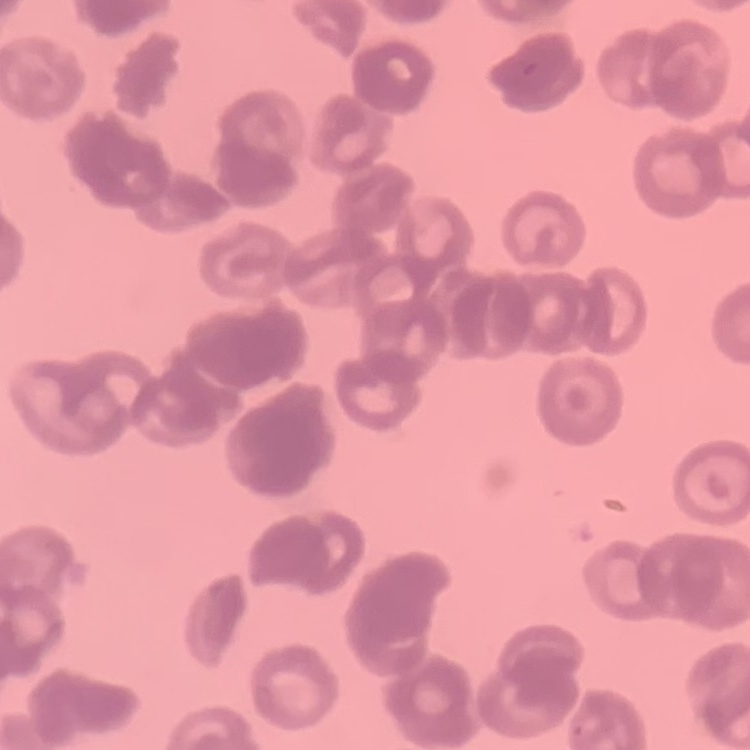

Summary:
  - Red blood cell morphology: rouleaux formation
  - Preparation: thin peripheral smear
  - Stain: Field's or Giemsa
  - Image type: square crop of a larger photomicrograph